State which parasite is depicted.
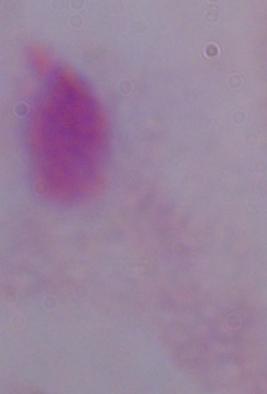
A trichomonad.

Summary:
  - Magnification: 1000x
  - Modality: photomicrograph